Identify the parasite.
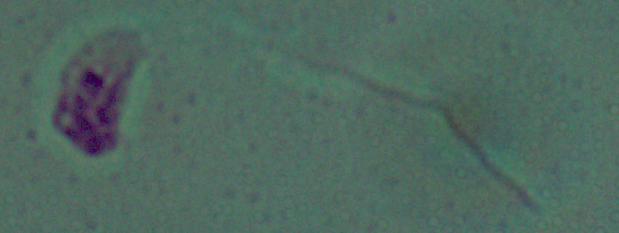

This is Leishmania.

Summary:
  - Magnification: 1000x
  - Modality: photomicrograph